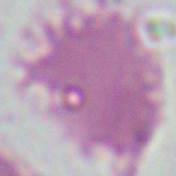
modality = photomicrograph
identification = red blood cell
magnification = 1000x